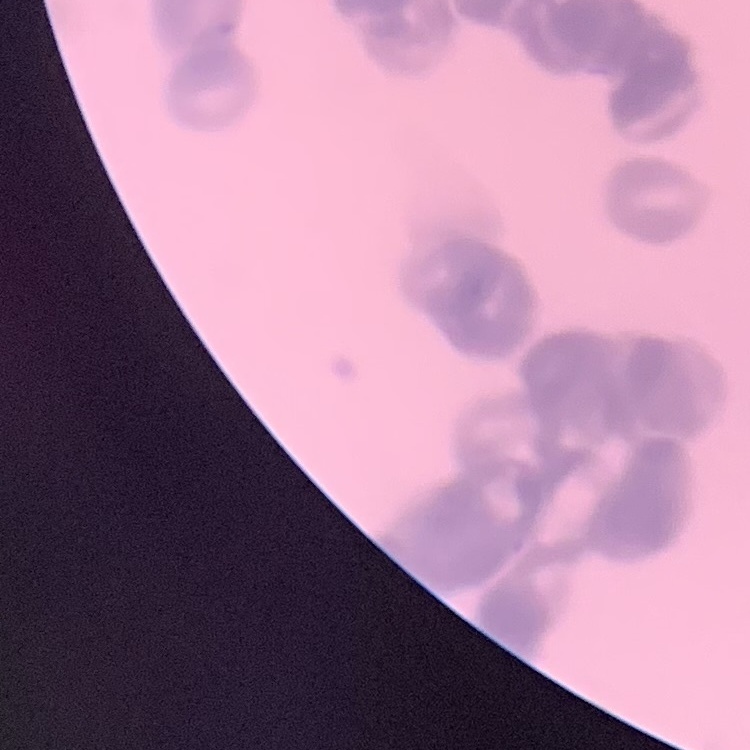
The red blood cells exhibit rouleaux formation. One tile cut from a larger photomicrograph. Thin blood smear. Stained with either Field's or Giemsa.